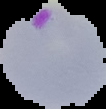

malaria status = parasitized
image type = cell region segmented out of the field of view; surrounding area masked to black
image size = 106×109 pixels
preparation = thin blood smear